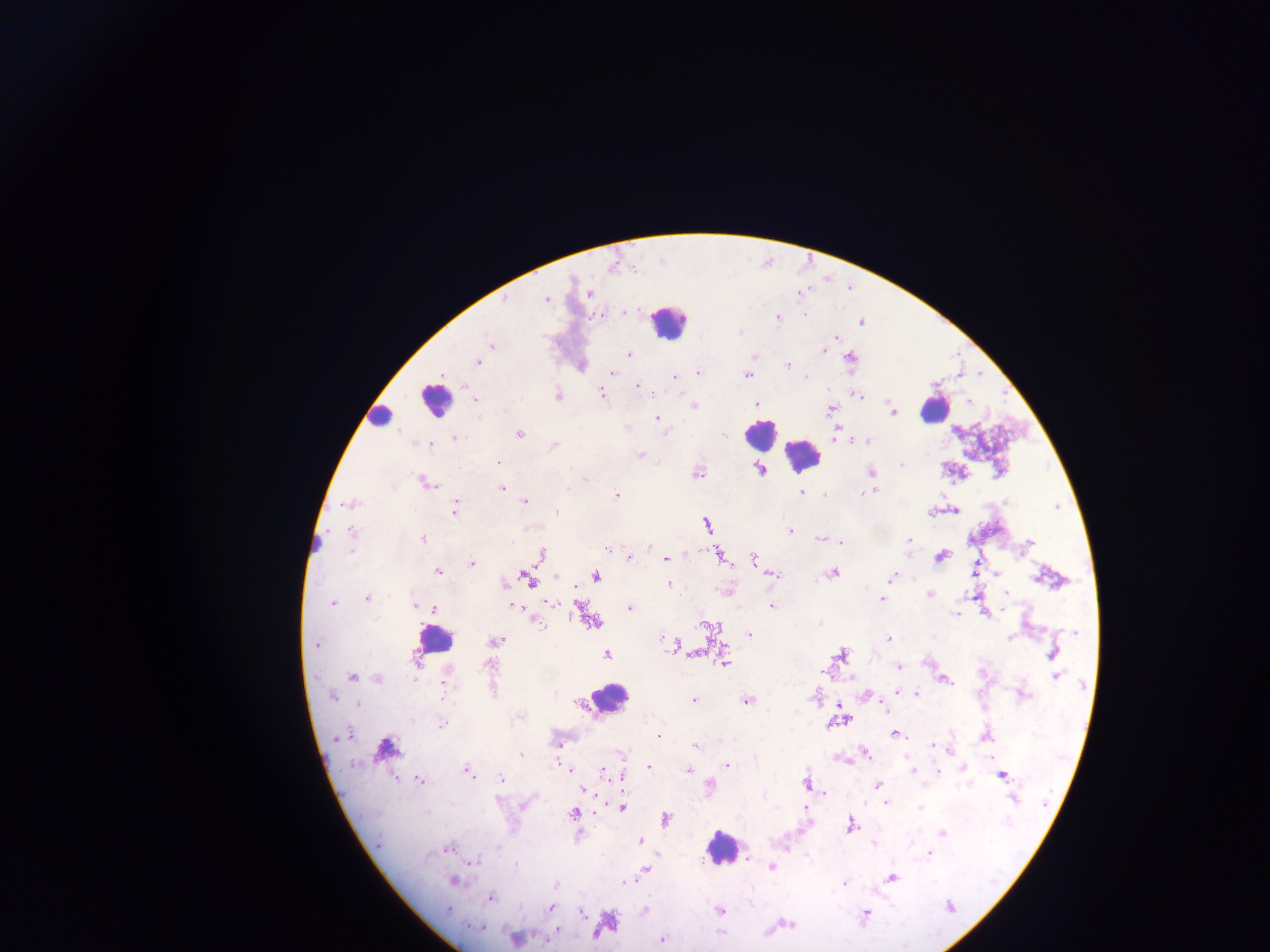
field of view = single
capture = mobile-phone photograph through a microscope
image size = 1270×952 pixels
leukocyte locations = approximate centers as [x, y] in pixels: [669, 321], [434, 399], [934, 409], [379, 418], [760, 435], [803, 455], [315, 543], [434, 640], [608, 698], [722, 849]
preparation = thick blood film
country = Ghana
Plasmodium parasite locations = approximate centers as [x, y] in pixels: [612, 267], [588, 293], [546, 300], [504, 301], [623, 311], [805, 315], [777, 318], [861, 321], [739, 332], [836, 337], [492, 345], [823, 350], [629, 354], [850, 358], [477, 362], [787, 366], [612, 372], [698, 372], [747, 375], [674, 377], [806, 377], [637, 386], [602, 393], [558, 396], [859, 396], [475, 399], [969, 401], [757, 403], [693, 405], [830, 409], [892, 411], [656, 417], [665, 432], [836, 432], [520, 434], [455, 437], [866, 442], [430, 445], [553, 446], [640, 455], [497, 462], [901, 465], [760, 469], [697, 472], [871, 472], [586, 480], [427, 483], [502, 488], [568, 488], [874, 491], [801, 492], [868, 492], [825, 494], [616, 495], [525, 501], [1007, 501], [350, 504], [455, 508], [956, 510], [557, 512], [932, 512], [707, 525], [790, 531], [351, 532], [422, 539], [820, 539], [908, 539], [840, 542], [1028, 543], [606, 548], [649, 548], [542, 555], [719, 556], [628, 557], [940, 557], [666, 559], [755, 560], [472, 563], [438, 571], [832, 573], [998, 574], [774, 575], [556, 576], [892, 576], [596, 577], [528, 579], [504, 584], [669, 585], [1006, 593], [930, 595], [367, 598], [882, 600], [332, 603], [549, 603], [415, 604], [772, 605], [513, 606], [630, 608], [433, 609], [956, 615], [536, 620], [592, 622], [819, 623], [709, 627], [1076, 632], [749, 635], [1011, 637], [662, 638], [888, 638], [495, 641], [316, 644], [675, 646], [681, 649], [694, 654], [1053, 654], [607, 655], [840, 655], [724, 662], [490, 665], [899, 667], [1056, 676], [352, 677], [378, 679], [946, 680], [446, 683], [897, 691], [917, 693], [1023, 695], [332, 697], [693, 700], [746, 700], [357, 704], [885, 707], [838, 721], [443, 725], [894, 734], [345, 735], [659, 736], [985, 737], [558, 744], [696, 745], [933, 745], [386, 748], [864, 753], [521, 754], [621, 754], [728, 765], [649, 767], [964, 768], [570, 770], [688, 770], [468, 771], [913, 771], [939, 771], [604, 772], [1004, 775], [501, 778], [420, 780], [807, 783], [878, 785], [709, 787], [584, 790], [1014, 798], [524, 803], [886, 803], [621, 807], [806, 808], [920, 808], [573, 814], [666, 820], [850, 826], [942, 832], [641, 840], [873, 844], [497, 847], [447, 848], [931, 854], [475, 862], [772, 867], [646, 868], [891, 879], [454, 880], [628, 882], [843, 883], [555, 886], [491, 898], [950, 907], [551, 908], [449, 910], [645, 910], [719, 911], [582, 913], [866, 914], [610, 923], [788, 924], [475, 927], [558, 931], [720, 933], [516, 939], [663, 939]